Classify this cell by malaria status.
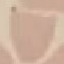

It is uninfected.

Summary:
  - Preparation: thin blood smear
  - Stain: Giemsa
  - Capture: smartphone through the microscope eyepiece
  - Image type: cell patch, automatically extracted from a larger field of view and resized to 64 × 64 pixels